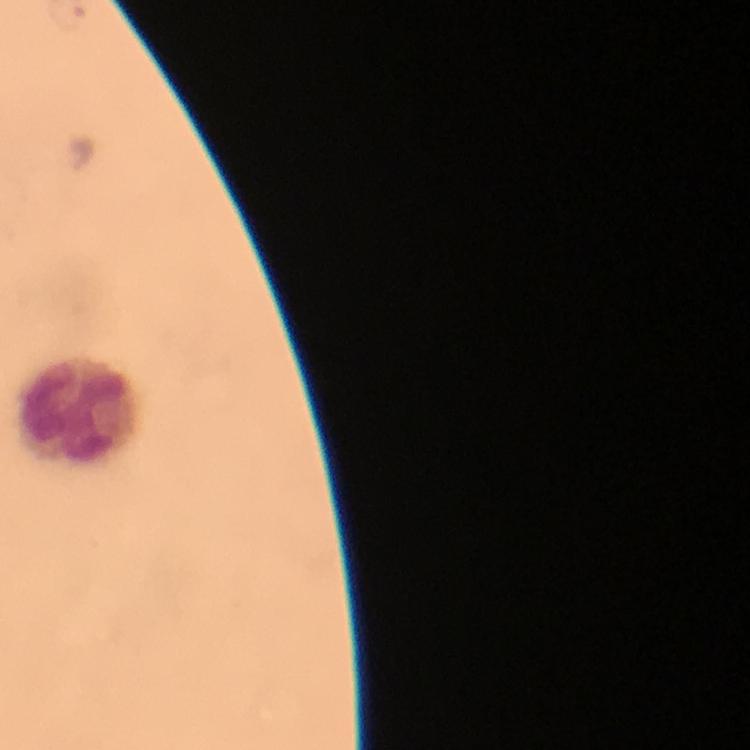

Approximate object centers, in pixels from the top-left corner.
Summary:
  - Leukocyte locations: (x=76, y=413)
  - Malaria parasites: none seen
  - Immersion oil: used
  - Stain: Giemsa
  - Preparation: thick blood film
  - Capture: smartphone mounted on the microscope
  - Cropped from: a single field of view
  - Image size: 750×750 pixels
  - Magnification: 100x
  - Context: from a diagnostic examination for malaria